Outline each blood parasite and name the species.
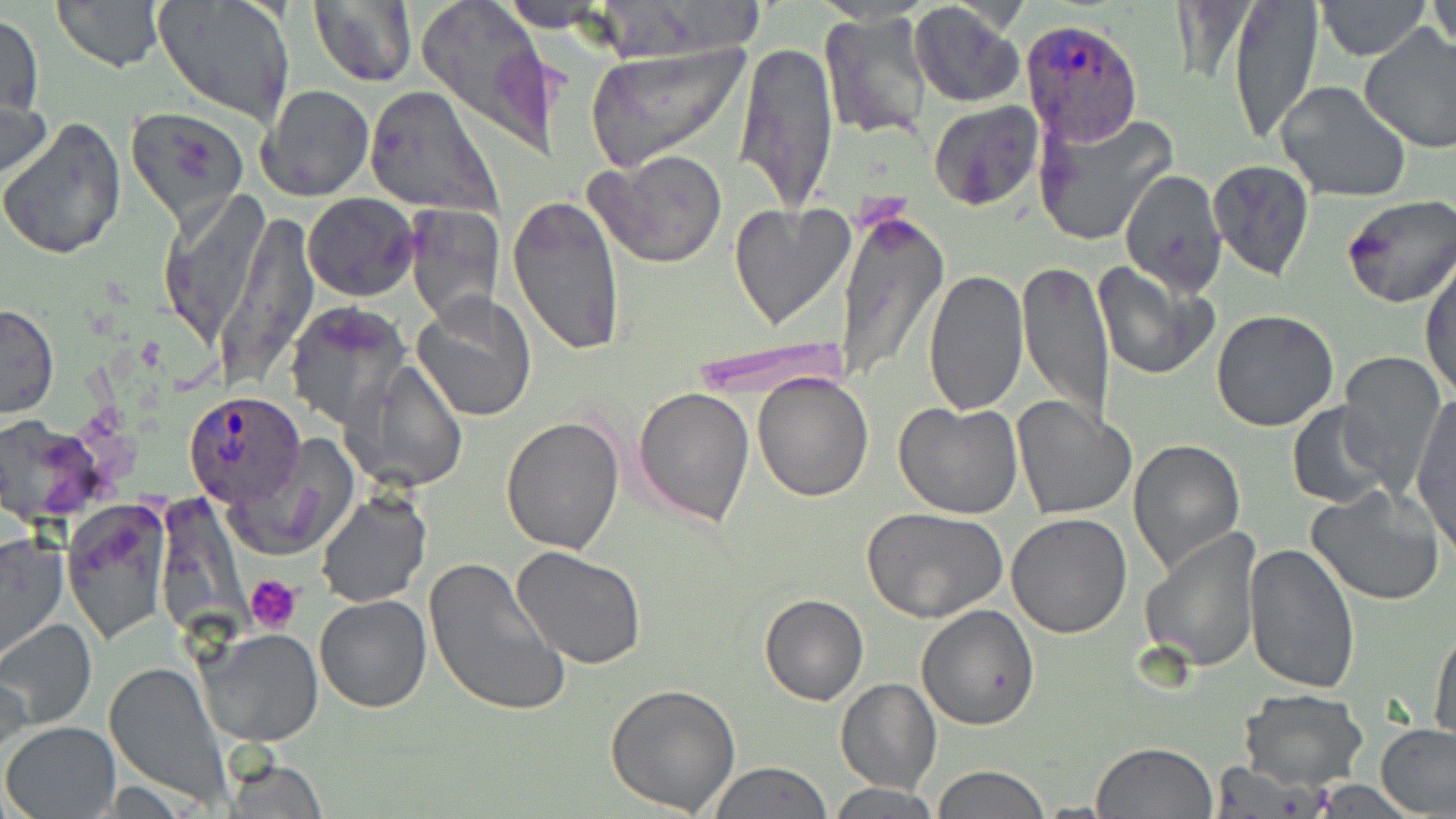
Approximate bounding boxes as [x1, y1, x2, y2] in pixels.
Plasmodium ovale-infected red blood cells: [1020, 17, 1145, 145], [182, 392, 309, 510].
No Plasmodium falciparum, Plasmodium malariae, Plasmodium vivax, Babesia divergens, or Trypanosoma brucei observed.

Platelet locations: [245, 574, 304, 633]. Uninfected red blood cell locations: [50, 0, 168, 72], [309, 0, 417, 89], [414, 0, 562, 156], [500, 0, 603, 26], [1226, 0, 1323, 144], [1314, 0, 1432, 61], [151, 1, 295, 126], [1429, 1, 1455, 59], [910, 2, 1025, 108], [820, 9, 932, 142], [1, 12, 44, 120], [1360, 25, 1456, 154], [734, 40, 840, 213], [583, 42, 750, 172], [0, 80, 52, 196], [1276, 81, 1413, 205], [259, 84, 375, 201], [365, 86, 499, 215], [928, 100, 1043, 211], [125, 106, 250, 228], [1033, 109, 1178, 245], [0, 118, 127, 259], [589, 149, 729, 269], [1208, 160, 1314, 281], [1120, 170, 1226, 293], [303, 193, 418, 302], [506, 194, 627, 357], [1338, 195, 1456, 309], [729, 201, 853, 329], [403, 205, 506, 323], [834, 207, 947, 384], [1421, 258, 1455, 398], [1017, 259, 1113, 430], [1094, 261, 1219, 381], [922, 270, 1028, 415], [411, 293, 537, 422], [284, 301, 410, 427], [0, 303, 59, 419], [1210, 309, 1340, 432], [1336, 351, 1446, 487], [346, 362, 467, 493], [753, 372, 873, 502], [632, 386, 756, 527], [1010, 396, 1132, 520], [1412, 396, 1455, 552], [894, 399, 1023, 518], [1286, 402, 1397, 508], [0, 414, 110, 525], [501, 415, 624, 554], [230, 439, 354, 560], [1129, 439, 1246, 577], [1305, 484, 1447, 605], [316, 492, 429, 607], [61, 504, 170, 644], [863, 506, 1008, 622], [1005, 514, 1132, 637], [1140, 527, 1259, 673], [0, 530, 69, 664], [1244, 542, 1361, 694], [511, 547, 646, 669], [423, 557, 570, 717], [314, 594, 431, 713], [759, 594, 868, 705], [916, 604, 1039, 731], [0, 619, 99, 730], [1430, 626, 1456, 743], [197, 628, 323, 746], [105, 660, 231, 806], [0, 667, 30, 767], [836, 678, 941, 795], [606, 682, 741, 815], [1236, 689, 1368, 790], [3, 722, 120, 817], [1376, 723, 1456, 816], [1092, 741, 1218, 818], [217, 751, 329, 818], [709, 761, 833, 818], [1211, 763, 1330, 817], [931, 766, 1050, 819], [829, 781, 941, 818]. Slide-level diagnosis: Plasmodium ovale. Light microscopy. May-Grünwald-Giemsa stain. Single field of view. Thin blood smear. 1000x magnification. Image is 1456×819 pixels.